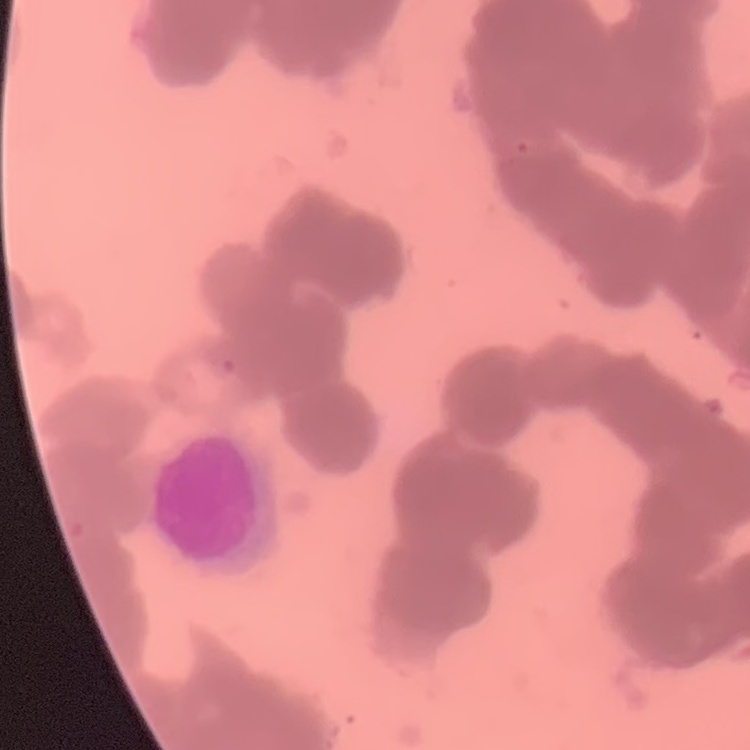
erythrocyte_morphology: rouleaux formation
image_type: square crop of a larger photomicrograph
preparation: thin peripheral smear
stain: Field's or Giemsa